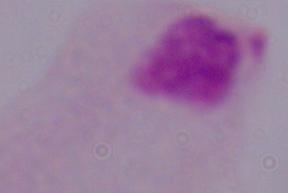

Summary:
  - Magnification: 1000x
  - Identification: trichomonad
  - Modality: photomicrograph